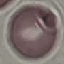

Summary:
  - Result: no malaria parasites seen
  - Image type: cell patch, automatically extracted from a larger field of view and resized to 64 × 64 pixels
  - Capture: smartphone camera at the microscope eyepiece
  - Preparation: thin blood smear
  - Stain: Giemsa